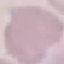
Summary:
  - Result: negative for malaria parasites
  - Capture: smartphone camera at the microscope eyepiece
  - Preparation: thin smear
  - Stain: Giemsa
  - Image type: cell patch, automatically extracted from a larger field of view and resized to 64 × 64 pixels